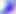
Toxoplasma gondii is shown. Captured at 400x magnification. Micrograph.